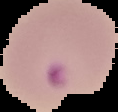
Summary:
  - Result: malaria parasites identified
  - Image type: segmented cell region with the area outside set to black
  - Preparation: thin blood film
  - Image size: 118×112 pixels